Assess this cell for malaria.
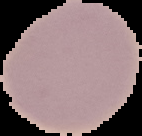

Uninfected.

Image is 142×136 pixels. From a thin blood film. Cell region segmented out of the field of view; the surrounding area is masked to black.